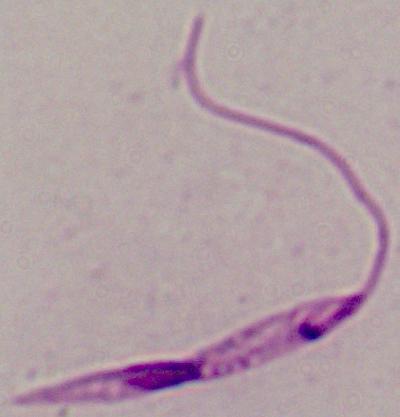
Summary:
  - Identification: Leishmania
  - Magnification: 1000x
  - Modality: micrograph